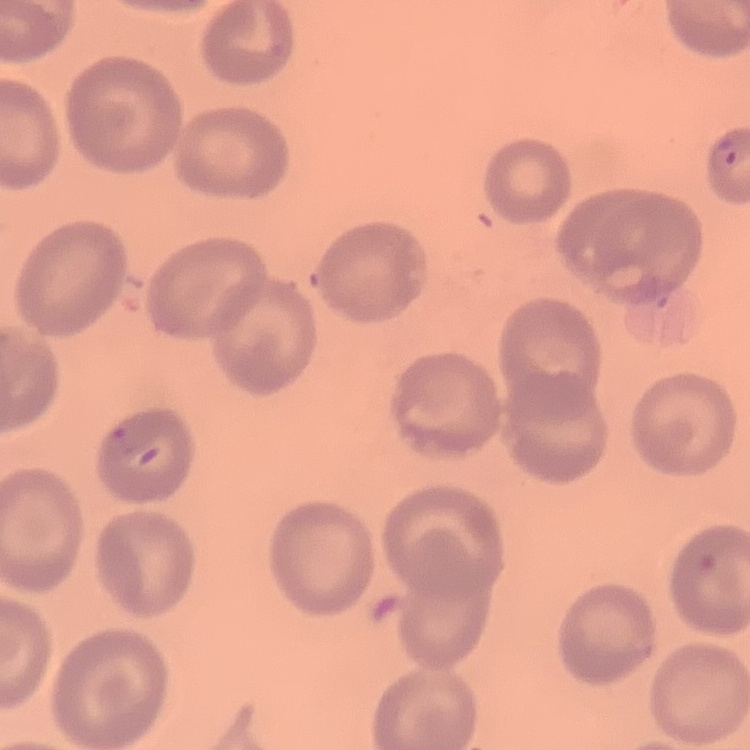

Summary:
  - Red blood cell morphology: no rouleaux formation
  - Stain: Field's or Giemsa
  - Preparation: thin peripheral smear
  - Image type: one tile cut from a larger photomicrograph